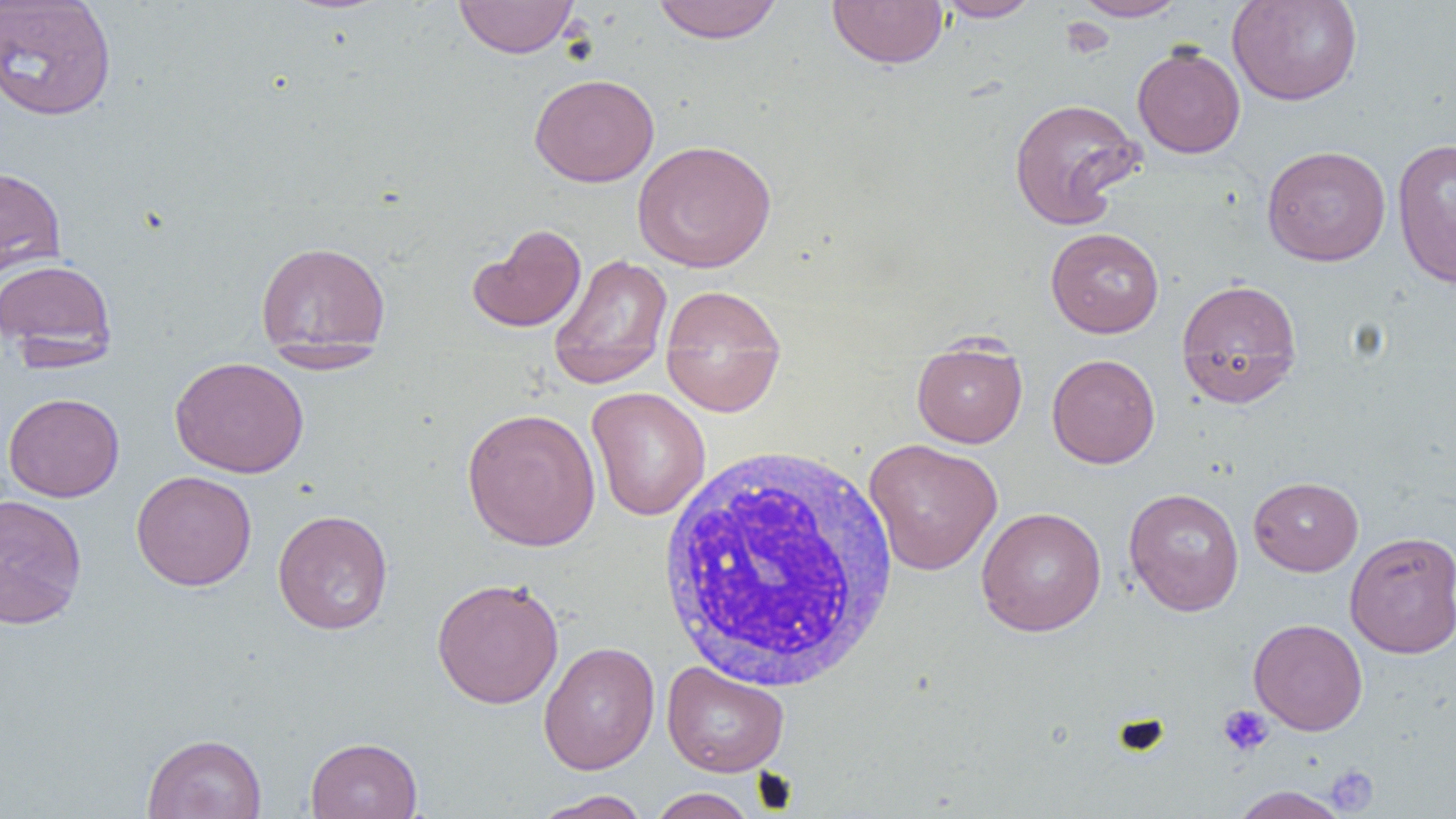
{
  "slide_level_diagnosis": "negative for blood parasites",
  "field_of_view": "single",
  "magnification": "1000x",
  "uninfected_red_blood_cell_locations": "approximate bounding boxes as (x1,y1)-(x2,y2) corner pairs in pixels: (0,0)-(117,121), (454,0)-(579,58), (652,0)-(783,44), (827,0)-(948,69), (935,0)-(1043,22), (1071,0)-(1190,21), (1227,0)-(1363,106), (1132,44)-(1245,158), (529,73)-(660,187), (1008,96)-(1144,228), (1392,138)-(1456,289), (632,139)-(777,273), (1261,145)-(1391,266), (0,165)-(67,279), (468,223)-(587,333), (1045,227)-(1164,338), (255,241)-(392,357), (548,253)-(673,389), (0,257)-(118,366), (1176,277)-(1303,408), (659,284)-(787,417), (911,338)-(1028,448), (260,343)-(390,373), (1046,353)-(1160,469), (169,356)-(309,478), (586,387)-(711,521), (3,392)-(124,502), (461,407)-(601,552), (863,438)-(1003,575), (131,470)-(257,591), (1248,476)-(1363,576), (1123,487)-(1245,616), (0,493)-(87,629), (976,506)-(1107,637), (272,509)-(393,635), (1344,530)-(1456,658), (431,577)-(565,709), (1248,618)-(1368,735), (539,641)-(660,775), (662,661)-(789,777), (142,732)-(267,819), (306,736)-(423,819), (1230,785)-(1350,819), (647,788)-(757,819), (532,790)-(652,819)",
  "modality": "optical microscopy",
  "white_blood_cell_locations": "approximate bounding boxes as (x1,y1)-(x2,y2) corner pairs in pixels: (655,443)-(903,693)",
  "image_size": "1456×819 pixels",
  "platelet_locations": "approximate bounding boxes as (x1,y1)-(x2,y2) corner pairs in pixels: (1218,704)-(1274,757), (1325,765)-(1379,815)",
  "preparation": "thin blood film"
}